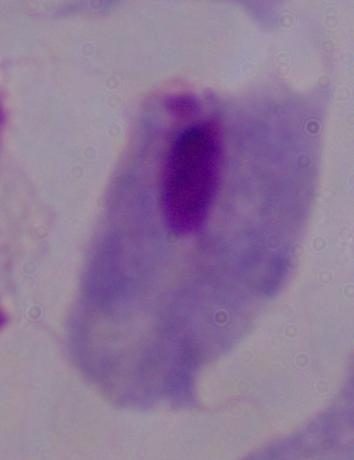

modality = micrograph
identification = trichomonad
magnification = 1000x